Assess the morphology of the red blood cells.
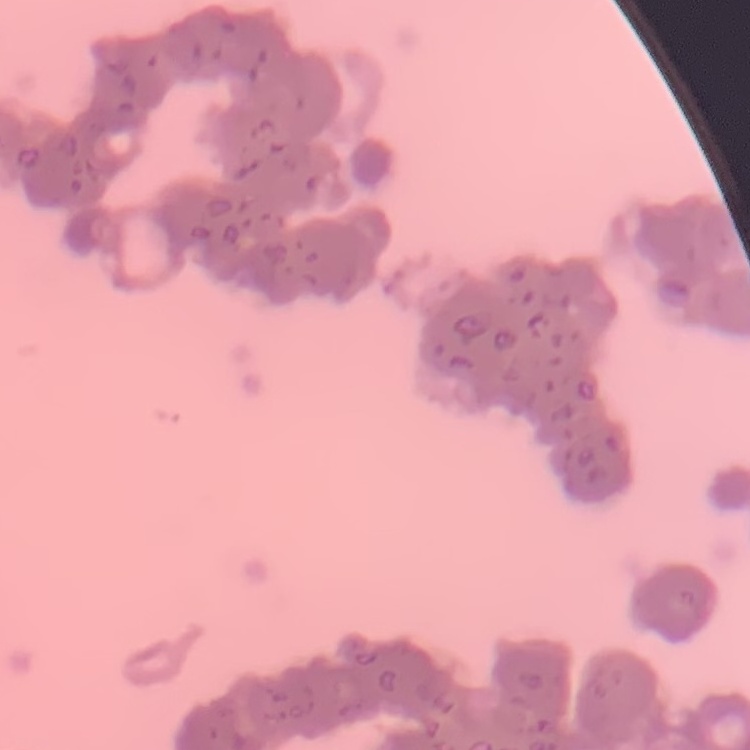

Rouleaux formation.

Square crop of a larger photomicrograph. Field's or Giemsa stain. Thin blood smear.